Name the parasite shown.
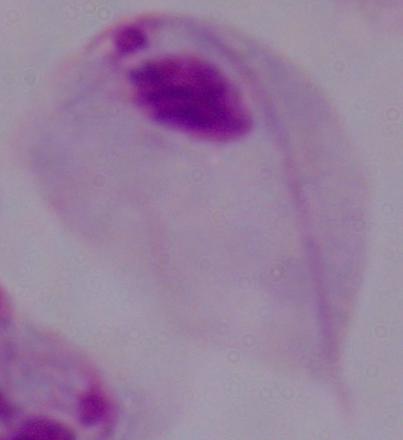
A trichomonad.

Photomicrograph. Captured at 1000x magnification.